Assess this cell for malaria.
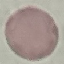
Uninfected.

{
  "preparation": "thin blood smear",
  "image_type": "automatically extracted cell patch, resized to 64 × 64 pixels",
  "capture": "smartphone through the microscope eyepiece",
  "stain": "Giemsa"
}